Identify the blood parasite species.
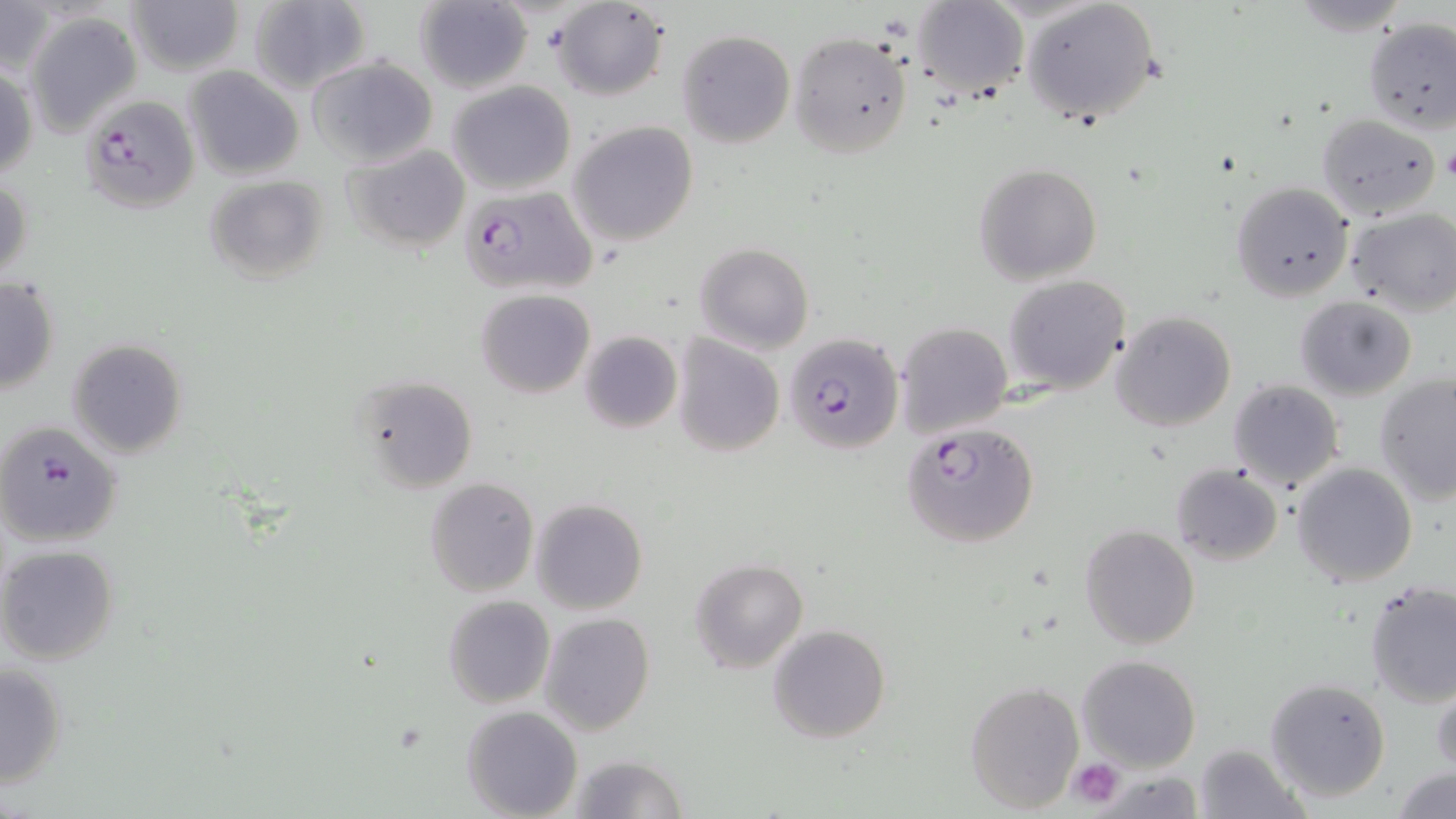
Plasmodium falciparum.

Approximate bounding boxes as named x1/y1/x2/y2 corners in pixels. Plasmodium falciparum-infected red blood cell locations: (x1=80, y1=93, x2=202, y2=213), (x1=461, y1=186, x2=597, y2=297), (x1=785, y1=335, x2=904, y2=454), (x1=0, y1=419, x2=123, y2=546), (x1=903, y1=423, x2=1040, y2=548). Uninfected red blood cell locations: (x1=550, y1=0, x2=669, y2=100), (x1=1020, y1=0, x2=1160, y2=127), (x1=0, y1=1, x2=55, y2=81), (x1=126, y1=1, x2=245, y2=76), (x1=248, y1=1, x2=372, y2=94), (x1=415, y1=1, x2=534, y2=94), (x1=912, y1=1, x2=1028, y2=100), (x1=24, y1=11, x2=142, y2=135), (x1=1361, y1=17, x2=1456, y2=133), (x1=677, y1=30, x2=794, y2=148), (x1=788, y1=32, x2=913, y2=158), (x1=307, y1=55, x2=438, y2=168), (x1=0, y1=65, x2=38, y2=181), (x1=183, y1=66, x2=304, y2=180), (x1=448, y1=80, x2=576, y2=195), (x1=1314, y1=112, x2=1441, y2=219), (x1=568, y1=121, x2=699, y2=247), (x1=342, y1=143, x2=472, y2=254), (x1=974, y1=163, x2=1101, y2=284), (x1=203, y1=175, x2=330, y2=287), (x1=0, y1=176, x2=32, y2=288), (x1=1231, y1=181, x2=1354, y2=301), (x1=1346, y1=209, x2=1456, y2=316), (x1=695, y1=241, x2=814, y2=354), (x1=0, y1=274, x2=60, y2=394), (x1=1002, y1=274, x2=1131, y2=394), (x1=476, y1=289, x2=595, y2=397), (x1=1295, y1=295, x2=1418, y2=400), (x1=1110, y1=311, x2=1237, y2=431), (x1=895, y1=322, x2=1013, y2=438), (x1=579, y1=330, x2=682, y2=434), (x1=671, y1=333, x2=786, y2=458), (x1=67, y1=338, x2=188, y2=458), (x1=1375, y1=373, x2=1456, y2=504), (x1=356, y1=374, x2=480, y2=494), (x1=1228, y1=377, x2=1343, y2=492), (x1=1292, y1=462, x2=1418, y2=587), (x1=1171, y1=464, x2=1283, y2=566), (x1=425, y1=477, x2=538, y2=599), (x1=532, y1=499, x2=648, y2=615), (x1=1079, y1=525, x2=1200, y2=649), (x1=0, y1=544, x2=121, y2=665), (x1=689, y1=558, x2=809, y2=675), (x1=1363, y1=580, x2=1456, y2=707), (x1=442, y1=595, x2=554, y2=708), (x1=539, y1=612, x2=655, y2=735), (x1=768, y1=625, x2=891, y2=744), (x1=1075, y1=654, x2=1200, y2=771), (x1=0, y1=660, x2=68, y2=790), (x1=1431, y1=673, x2=1456, y2=777), (x1=1265, y1=676, x2=1390, y2=802), (x1=966, y1=680, x2=1083, y2=814), (x1=461, y1=704, x2=582, y2=818), (x1=1194, y1=743, x2=1304, y2=818), (x1=569, y1=754, x2=692, y2=818), (x1=1391, y1=766, x2=1455, y2=819). Platelet locations: (x1=1442, y1=146, x2=1456, y2=185), (x1=1068, y1=758, x2=1125, y2=808). 1000x magnification. One field of a larger specimen. Optical microscopy. Thin blood smear. Image is 1456×819 pixels. May-Grünwald-Giemsa-stained preparation.